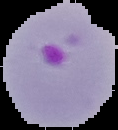
Image is 118×130 pixels. From a thin blood film. Result: Plasmodium parasites detected. The area outside the segmented cell region is set to black.